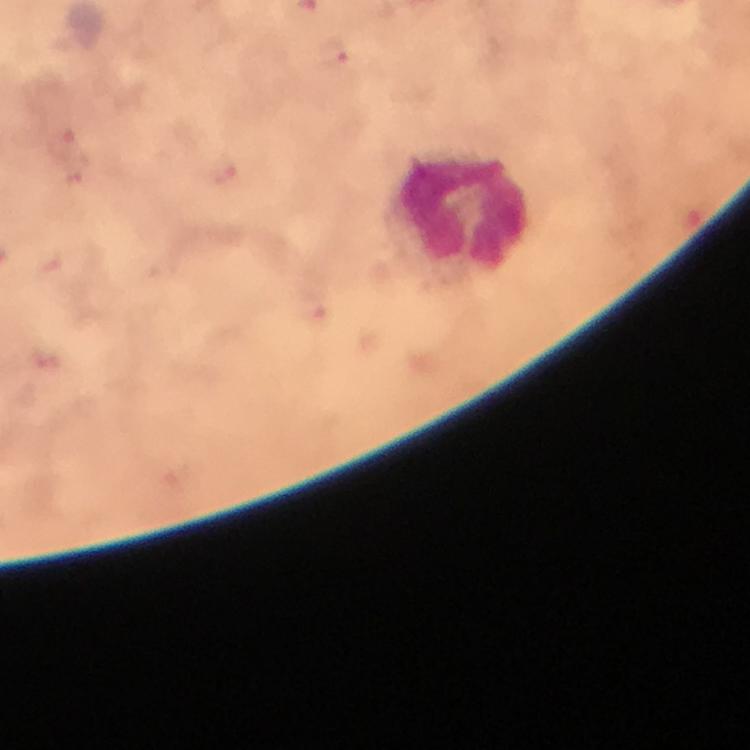
stain = Giemsa
magnification = 100x
image size = 750×750 pixels
leukocyte locations = approximate object centers, in pixels from the top-left corner: (x=460, y=215)
immersion oil = applied
preparation = thick smear
cropped from = a single field of view
malaria parasite locations = approximate object centers, in pixels from the top-left corner: (x=333, y=47), (x=66, y=145), (x=223, y=170)
context = from a diagnostic examination for malaria
capture = smartphone camera through the microscope